Report the malaria status of this cell.
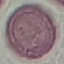
It is uninfected.

Thin blood film. Giemsa stain. Cell patch, automatically extracted from a larger field of view and resized to 64 × 64 pixels. Photographed with a smartphone camera at the microscope eyepiece.